Assess this cell for malaria.
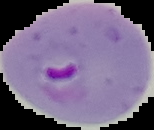
It is parasitized.

Image is 154×130 pixels. The area outside the segmented cell region is set to black. From a thin blood smear.